Look for Plasmodium parasites.
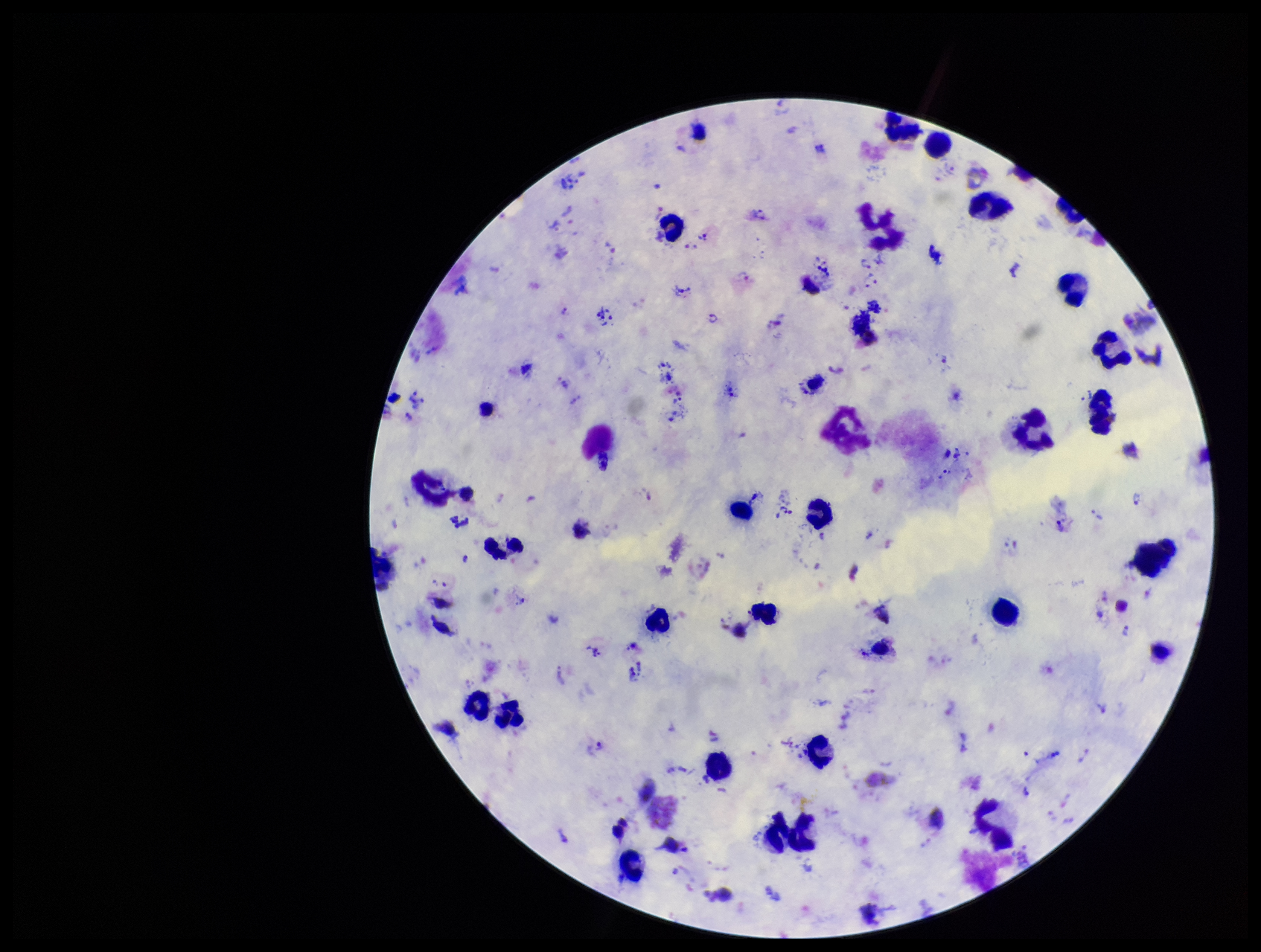

Detected.

image size = 1261×952 pixels
stain = Giemsa
species reported for this patient = Plasmodium vivax
leukocyte count = 29
field of view = single
preparation = thick blood smear
capture = smartphone photograph through the microscope eyepiece
patient malaria status = positive
parasite count = 38